Classify this cell by malaria status.
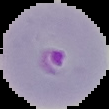
It is parasitized.

preparation: thin blood smear
image_type: segmented cell region with the area outside set to black
image_size: 109×109 pixels